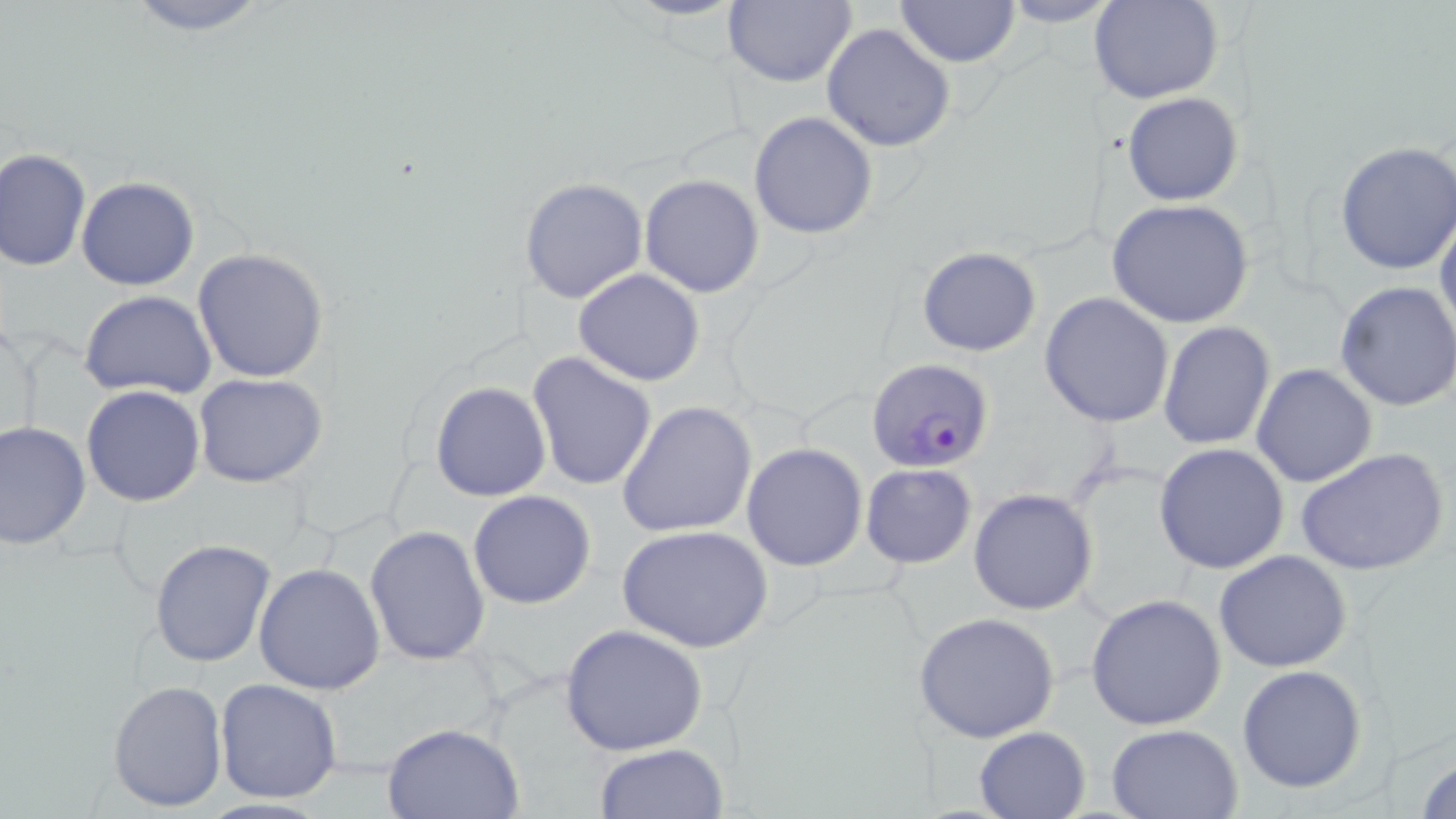

{
  "slide_level_diagnosis": "Plasmodium falciparum",
  "stain": "May-Grünwald-Giemsa",
  "preparation": "thin blood smear",
  "field_of_view": "one of a larger specimen",
  "magnification": "1000x",
  "image_size": "1456×819 pixels",
  "plasmodium_falciparum_infected_red_blood_cell_locations": "approximate bounding boxes as (x1,y1)-(x2,y2) corner pairs in pixels: (868,358)-(995,471)",
  "uninfected_red_blood_cell_locations": "approximate bounding boxes as (x1,y1)-(x2,y2) corner pairs in pixels: (116,0)-(278,37), (617,0)-(752,21), (724,0)-(856,87), (997,0)-(1124,27), (1090,0)-(1223,104), (893,1)-(1023,68), (821,23)-(955,152), (1121,92)-(1244,206), (748,111)-(878,240), (1335,138)-(1456,275), (1,148)-(91,272), (639,174)-(766,297), (78,176)-(200,290), (519,176)-(648,303), (1106,199)-(1254,327), (1434,205)-(1456,342), (916,246)-(1043,356), (192,247)-(331,383), (574,269)-(705,386), (1334,280)-(1456,413), (80,290)-(219,401), (1040,293)-(1173,428), (1157,321)-(1275,451), (0,325)-(44,454), (528,351)-(658,491), (1251,363)-(1378,487), (193,373)-(328,489), (430,381)-(552,502), (79,384)-(206,506), (617,401)-(755,539), (0,421)-(90,552), (1154,442)-(1292,576), (741,443)-(869,571), (1295,447)-(1450,578), (860,464)-(977,568), (968,488)-(1097,614), (468,490)-(596,609), (616,523)-(775,652), (365,525)-(491,667), (148,539)-(274,667), (1211,550)-(1354,674), (253,563)-(386,695), (1084,593)-(1227,731), (913,612)-(1062,742), (562,625)-(708,757), (1237,664)-(1365,793), (106,678)-(229,813), (215,678)-(343,805), (380,722)-(525,818), (1105,722)-(1245,818), (973,725)-(1092,818), (592,742)-(729,818), (1412,751)-(1456,818)",
  "modality": "light microscopy"
}